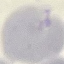

Summary:
  - Result: no malaria parasites detected
  - Capture: smartphone through the microscope eyepiece
  - Image type: cell patch, automatically extracted from a larger field of view and resized to 64 × 64 pixels
  - Preparation: thin smear
  - Stain: Giemsa